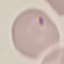

Malaria status: uninfected. Cell patch, automatically extracted from a larger field of view and resized to 64 × 64 pixels. Thin blood film. Giemsa-stained preparation. Acquired by smartphone through the microscope eyepiece.